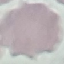

Summary:
  - Result: no malaria parasites seen
  - Image type: cell patch, automatically extracted from a larger field of view and resized to 64 × 64 pixels
  - Preparation: thin smear
  - Capture: smartphone camera at the microscope eyepiece
  - Stain: Giemsa